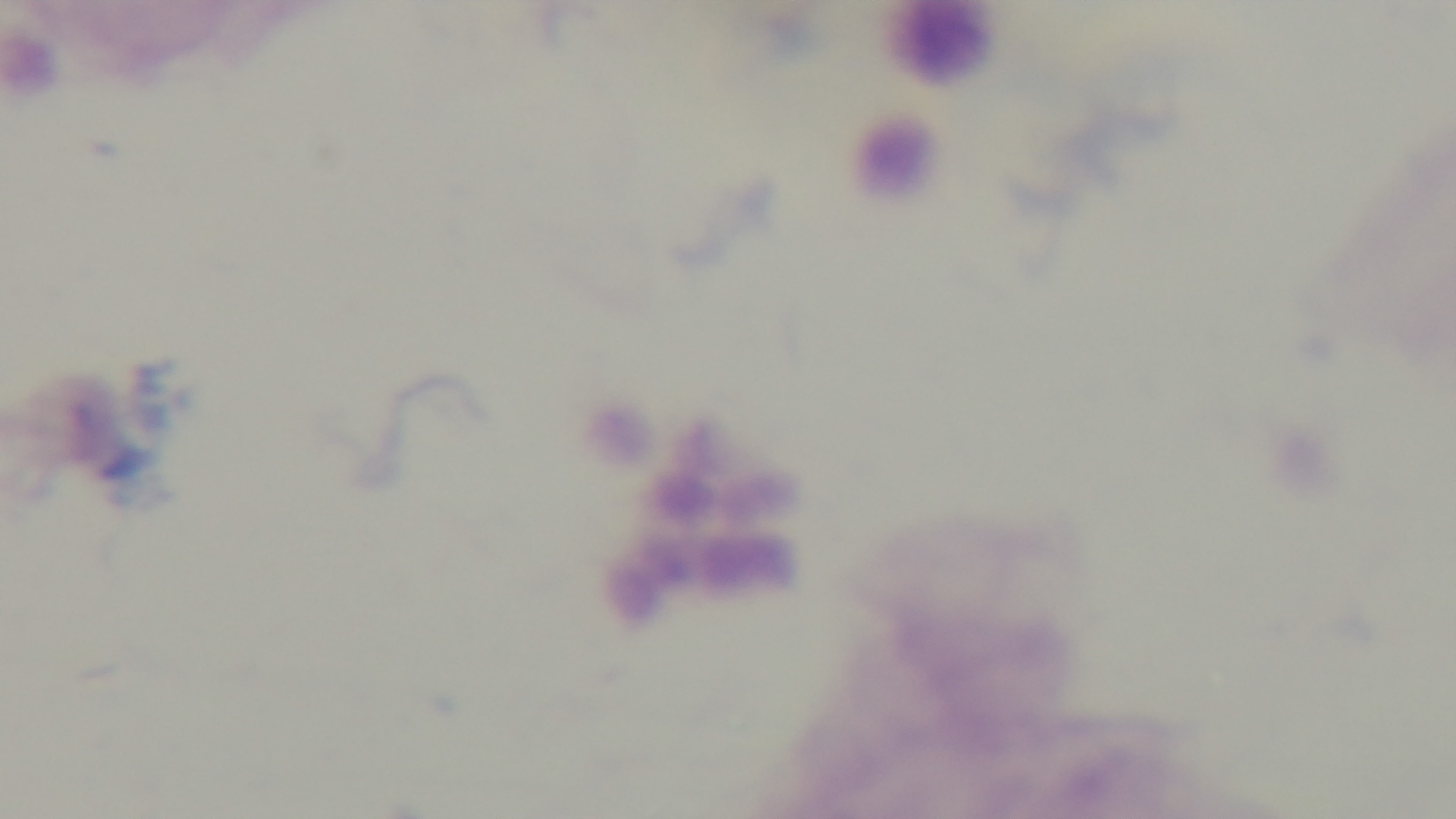
Malaria status: negative. 100x oil-immersion objective. Single field of view. Captured with a mounted 4K digital camera. Light microscopy. Giemsa-stained. Preparation: thick.